State which parasite is depicted.
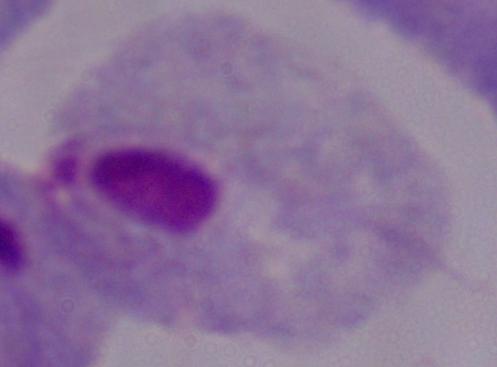

This is a trichomonad.

Summary:
  - Magnification: 1000x
  - Modality: micrograph